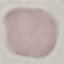
malaria status = uninfected
preparation = thin smear
capture = smartphone through the microscope eyepiece
image type = cell patch, automatically extracted from a larger field of view and resized to 64 × 64 pixels
stain = Giemsa